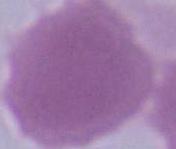
1000x magnification. Photomicrograph. A red blood cell is shown.